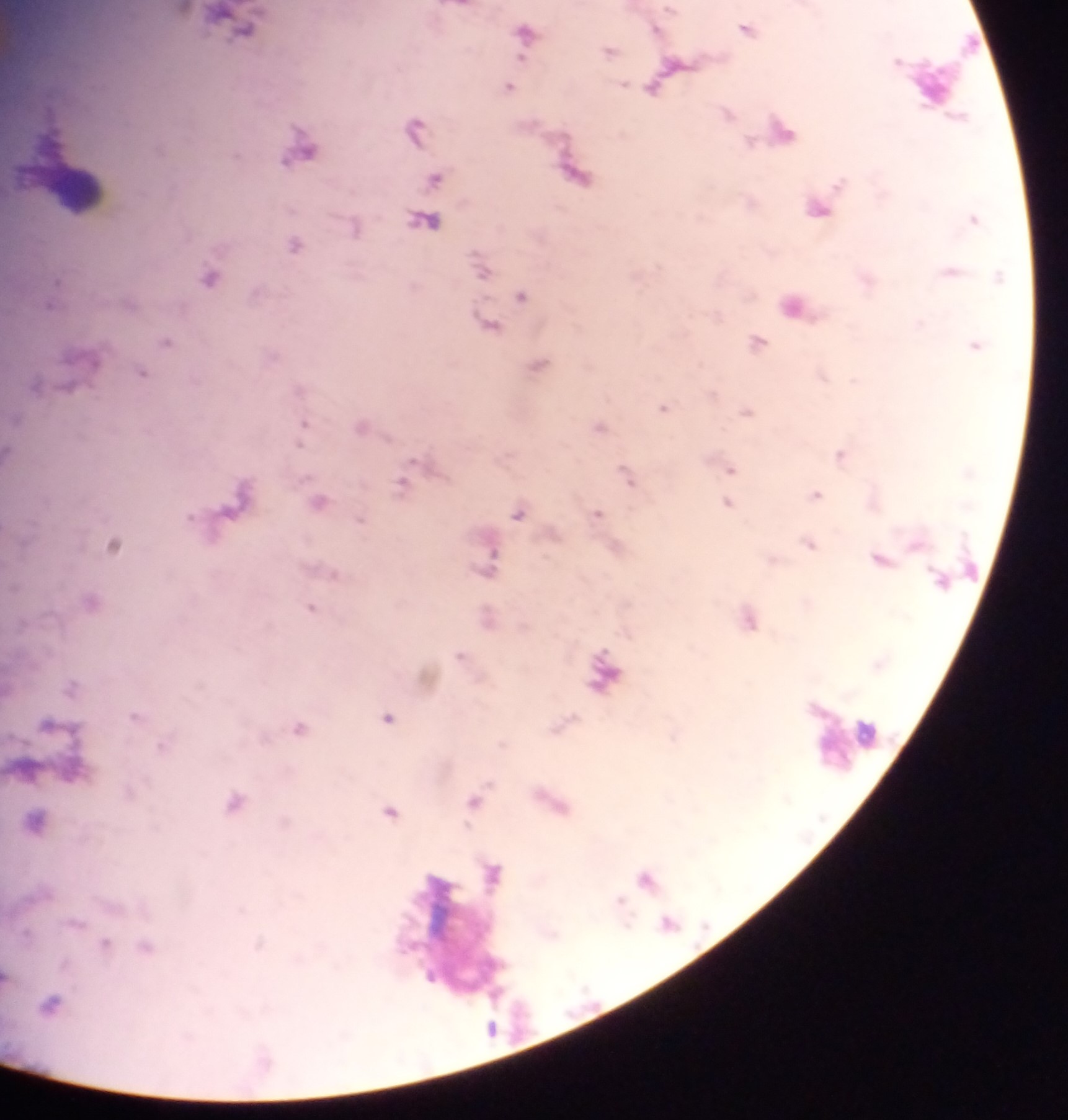

Approximate centers as [x, y] in pixels.
Summary:
  - Leukocyte locations: [74, 189], [847, 742]
  - Malaria parasite locations: [240, 26], [745, 29], [523, 32], [609, 51], [508, 87], [414, 129], [302, 149], [435, 179], [817, 208], [973, 219], [424, 221], [353, 227], [293, 245], [479, 266], [210, 277], [521, 296], [791, 306], [487, 324], [165, 341], [757, 341], [975, 345], [539, 365], [141, 372], [663, 408], [746, 411], [304, 423], [361, 425], [598, 427], [840, 455], [730, 469], [626, 477], [402, 484], [815, 494], [320, 501], [727, 503], [596, 513], [517, 514], [360, 521], [113, 544], [809, 545], [879, 559], [490, 560], [309, 607], [459, 655], [70, 686], [134, 715], [387, 717], [298, 728], [472, 801], [233, 802], [391, 811], [645, 879], [667, 922], [26, 933], [52, 1004]
  - Image size: 1068×1120 pixels
  - Country: Ghana
  - Preparation: thick blood smear
  - Field of view: single
  - Capture: mobile-phone photograph through a microscope